Report the malaria status of this cell.
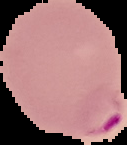
Parasitized.

From a thin blood film. Image is 127×145 pixels. Segmented cell region on a black background.